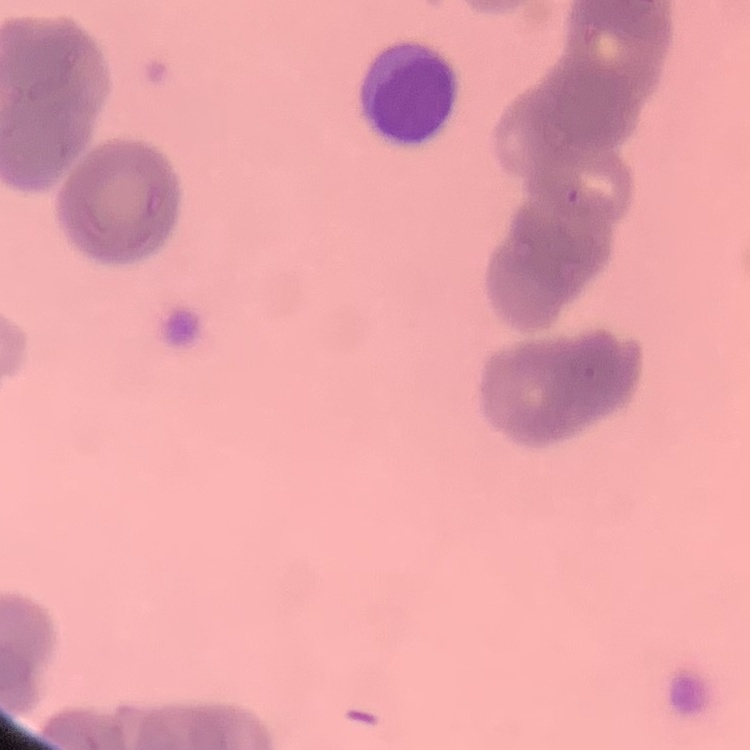

Summary:
  - Erythrocyte morphology: rouleaux formation
  - Stain: Field's or Giemsa
  - Image type: one tile cut from a larger photomicrograph
  - Preparation: thin blood film